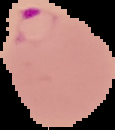

result = Plasmodium parasites detected
preparation = thin blood film
image size = 115×130 pixels
image type = segmented cell region with the area outside set to black